State the preparation type.
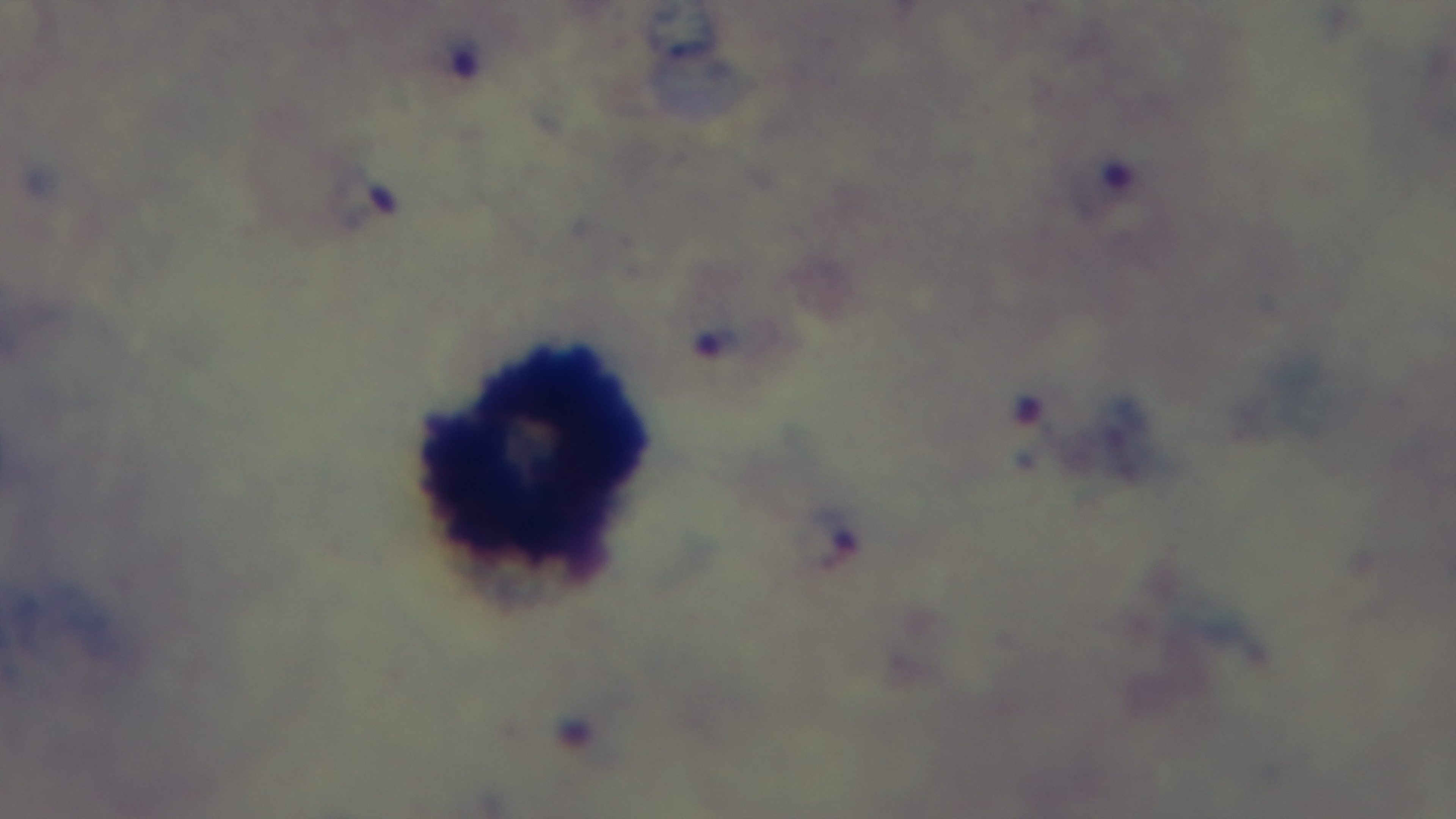

A thick smear.

Single field of view. Captured with a mounted 4K digital camera. Light microscopy. Malaria status: positive. Giemsa-stained. Oil-immersion objective, 100x.